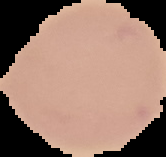 Segmented cell region on a black background. Image is 166×157 pixels. Result: negative for malaria parasites. From a thin blood smear.